Assess the morphology of the erythrocytes.
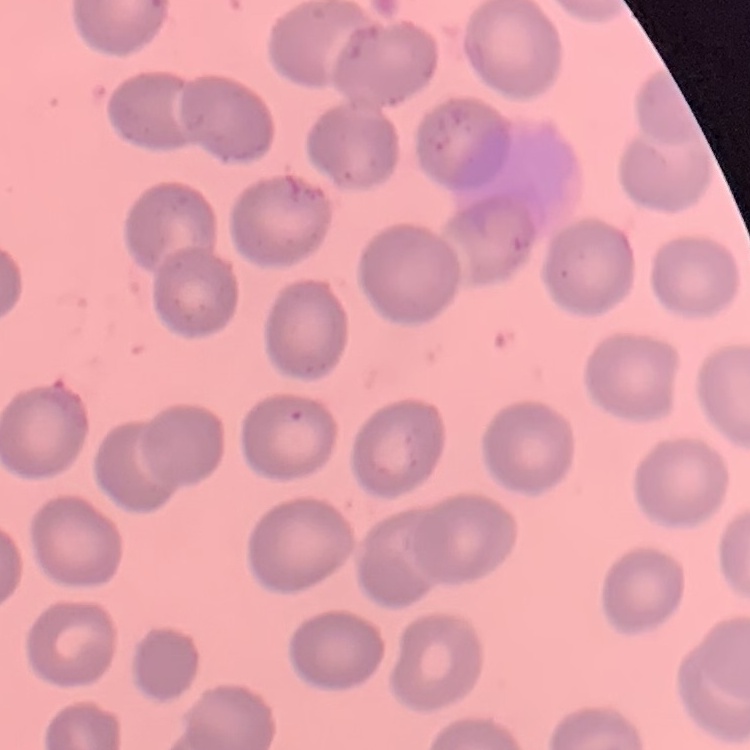
They show no rouleaux formation.

stain = Field's or Giemsa
preparation = thin blood film
image type = one tile cut from a larger photomicrograph